Evaluate for Plasmodium parasites.
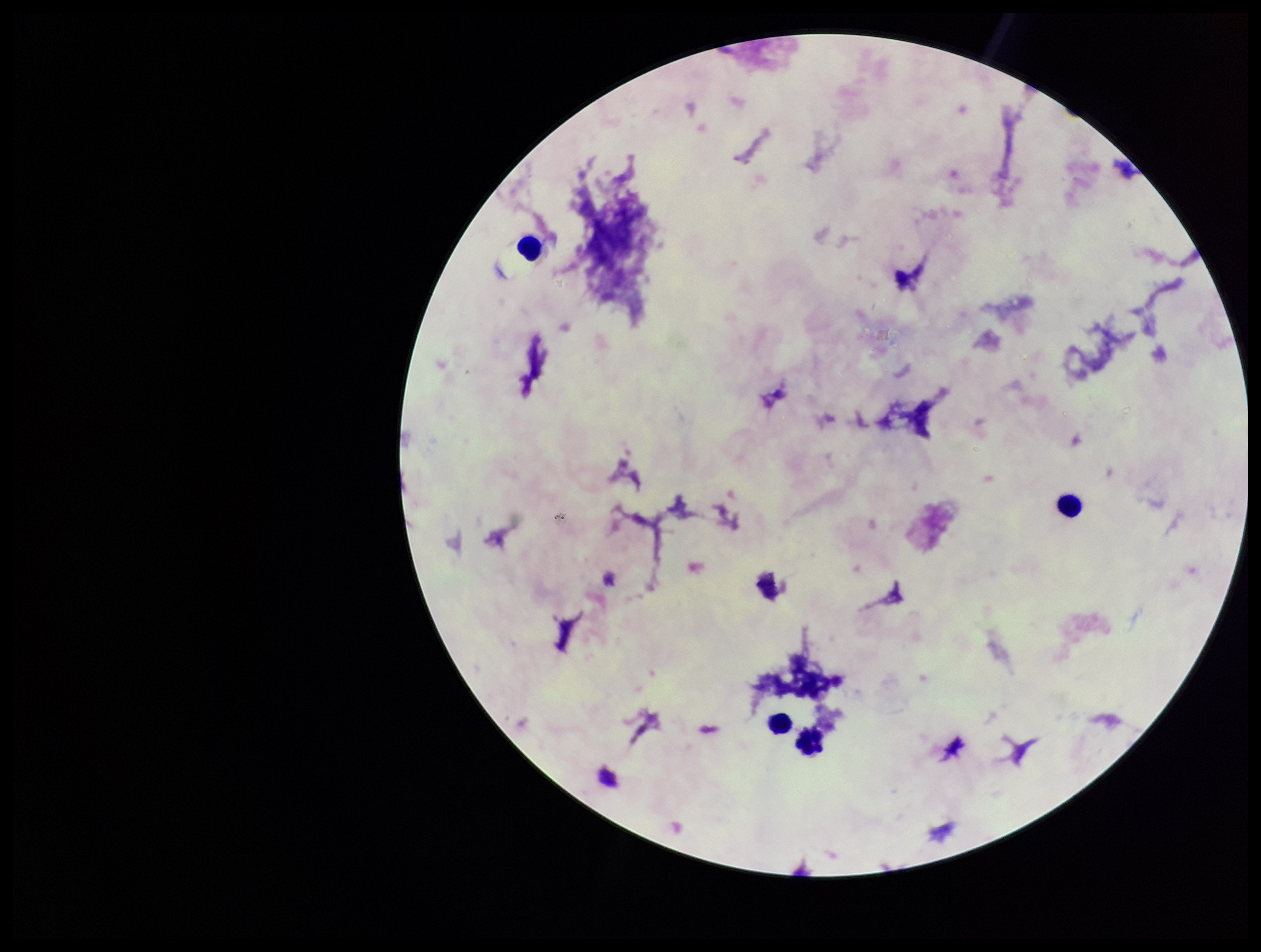

None identified.

patient malaria status = negative
parasite count = 0
leukocyte count = 4
field of view = single
stain = Giemsa
image size = 1261×952 pixels
preparation = thick
capture = smartphone photograph through the microscope eyepiece